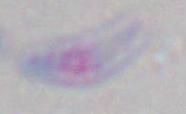
magnification = 1000x
modality = photomicrograph
identification = Toxoplasma gondii